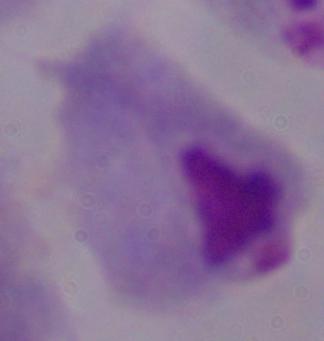

Summary:
  - Magnification: 1000x
  - Modality: photomicrograph
  - Identification: trichomonad